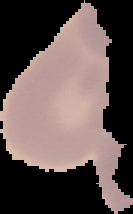

Summary:
  - Image type: segmented cell region on a black background
  - Image size: 133×214 pixels
  - Preparation: thin blood smear
  - Malaria status: uninfected